Locate every Plasmodium parasite and every leukocyte.
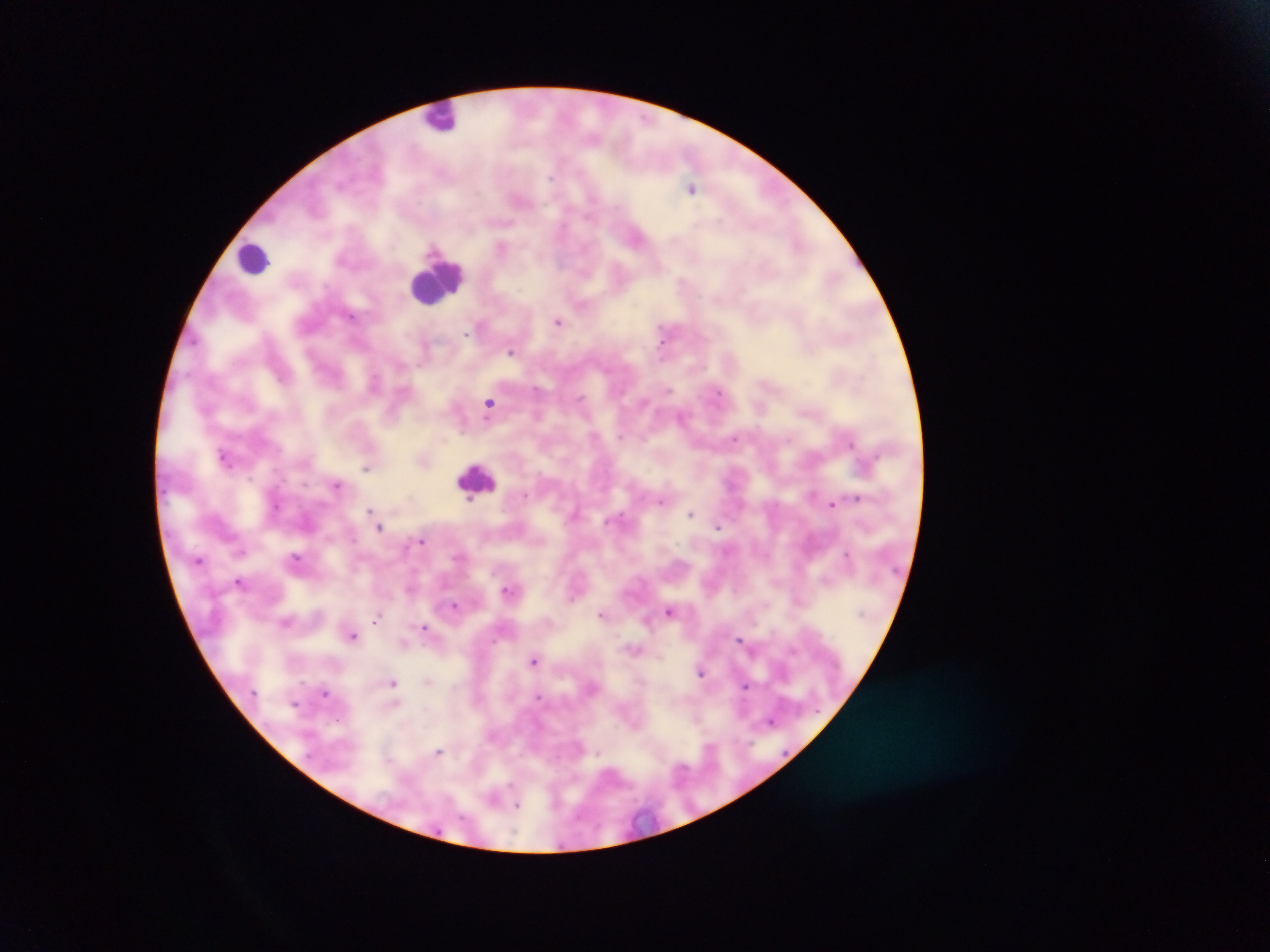

Approximate centers as {x, y} in pixels.
Plasmodium parasites: {551, 179}, {693, 188}, {661, 266}, {351, 315}, {559, 320}, {664, 329}, {467, 332}, {305, 343}, {511, 352}, {539, 388}, {668, 391}, {579, 399}, {489, 403}, {760, 407}, {681, 416}, {735, 438}, {850, 443}, {223, 452}, {366, 468}, {337, 484}, {525, 495}, {856, 497}, {828, 502}, {368, 510}, {691, 513}, {381, 527}, {718, 527}, {423, 543}, {242, 552}, {848, 554}, {296, 557}, {828, 578}, {240, 581}, {508, 590}, {575, 594}, {800, 601}, {456, 607}, {669, 610}, {603, 614}, {377, 618}, {284, 623}, {425, 627}, {353, 637}, {740, 638}, {794, 648}, {534, 660}, {701, 674}, {305, 677}, {393, 683}, {746, 685}, {326, 694}, {539, 696}, {696, 720}, {770, 721}, {711, 745}, {438, 750}, {599, 754}, {510, 785}, {519, 805}.
Leukocytes: {449, 111}, {249, 263}, {438, 288}, {475, 476}.

One field of view. Thick blood smear. Sample from Ghana. Image is 1270×952 pixels. Photographed through a microscope with a mobile-phone camera.